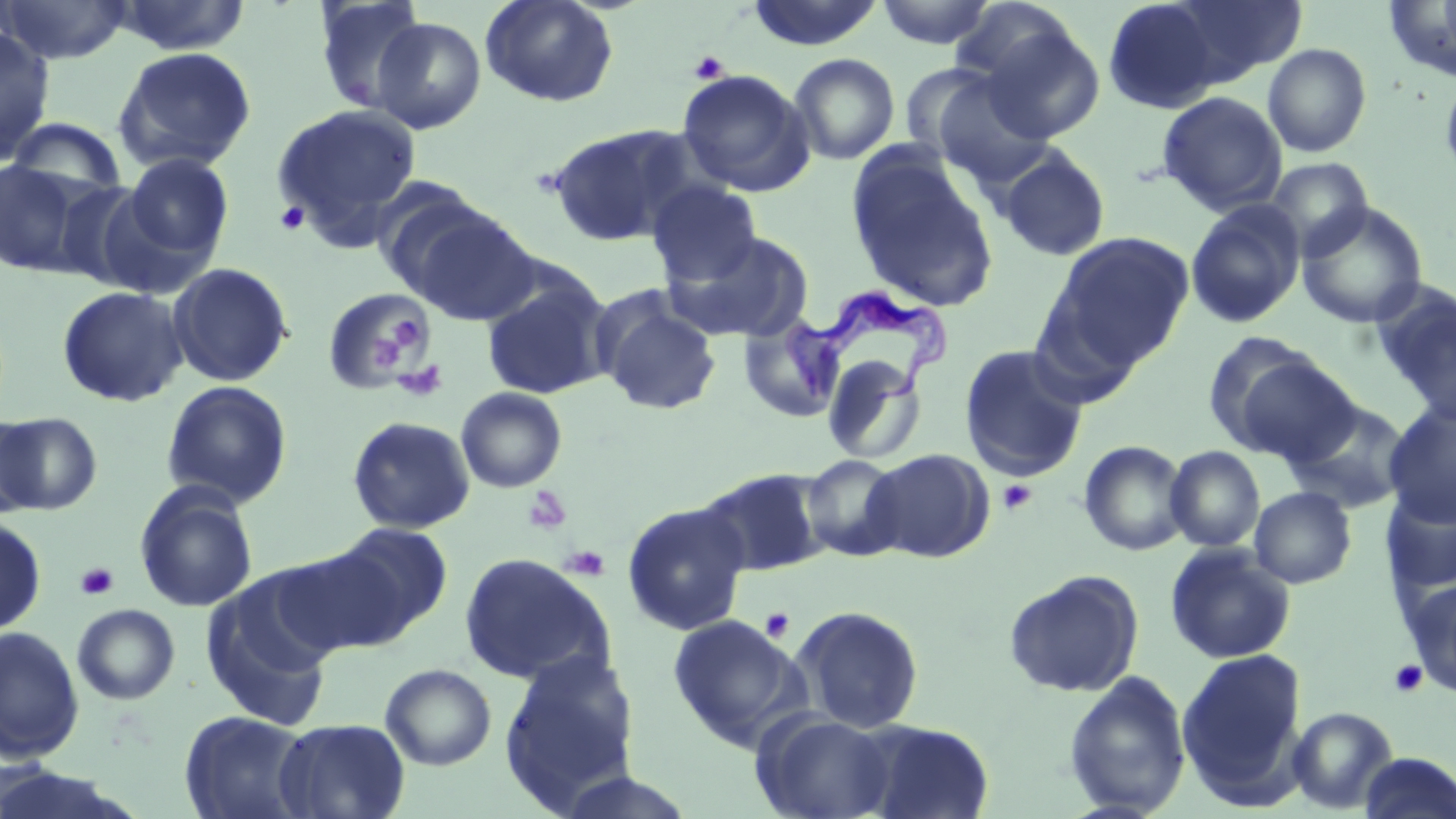
slide-level diagnosis = Trypanosoma brucei
uninfected red blood cell locations = approximate bounding boxes as named x1/y1/x2/y2 corners in pixels: (x1=109, y1=0, x2=252, y2=56), (x1=312, y1=0, x2=431, y2=115), (x1=480, y1=0, x2=619, y2=108), (x1=746, y1=0, x2=883, y2=51), (x1=875, y1=0, x2=996, y2=49), (x1=1102, y1=0, x2=1224, y2=113), (x1=1166, y1=0, x2=1307, y2=84), (x1=0, y1=1, x2=132, y2=64), (x1=950, y1=1, x2=1081, y2=90), (x1=1383, y1=3, x2=1456, y2=82), (x1=370, y1=17, x2=486, y2=134), (x1=0, y1=25, x2=55, y2=165), (x1=980, y1=25, x2=1106, y2=143), (x1=1262, y1=43, x2=1372, y2=158), (x1=113, y1=46, x2=257, y2=174), (x1=788, y1=53, x2=900, y2=165), (x1=1440, y1=66, x2=1456, y2=190), (x1=913, y1=67, x2=1057, y2=185), (x1=677, y1=69, x2=814, y2=196), (x1=1157, y1=91, x2=1287, y2=215), (x1=271, y1=102, x2=422, y2=244), (x1=5, y1=116, x2=129, y2=201), (x1=545, y1=123, x2=701, y2=246), (x1=997, y1=146, x2=1112, y2=260), (x1=846, y1=151, x2=999, y2=313), (x1=121, y1=153, x2=233, y2=265), (x1=1263, y1=156, x2=1374, y2=260), (x1=0, y1=159, x2=88, y2=278), (x1=647, y1=181, x2=762, y2=286), (x1=1185, y1=200, x2=1306, y2=329), (x1=1296, y1=202, x2=1429, y2=328), (x1=402, y1=204, x2=541, y2=325), (x1=667, y1=230, x2=814, y2=343), (x1=1047, y1=230, x2=1195, y2=370), (x1=167, y1=262, x2=294, y2=387), (x1=481, y1=275, x2=614, y2=399), (x1=1372, y1=283, x2=1456, y2=423), (x1=56, y1=285, x2=189, y2=408), (x1=320, y1=286, x2=432, y2=394), (x1=594, y1=293, x2=722, y2=417), (x1=738, y1=312, x2=848, y2=423), (x1=1205, y1=337, x2=1352, y2=463), (x1=958, y1=343, x2=1090, y2=481), (x1=822, y1=354, x2=927, y2=465), (x1=160, y1=380, x2=293, y2=509), (x1=456, y1=387, x2=567, y2=493), (x1=1284, y1=399, x2=1413, y2=515), (x1=1383, y1=402, x2=1456, y2=526), (x1=0, y1=412, x2=41, y2=519), (x1=1, y1=413, x2=101, y2=516), (x1=347, y1=416, x2=475, y2=534), (x1=1078, y1=439, x2=1191, y2=556), (x1=1165, y1=445, x2=1265, y2=551), (x1=862, y1=448, x2=994, y2=562), (x1=801, y1=455, x2=905, y2=561), (x1=697, y1=467, x2=830, y2=578), (x1=134, y1=483, x2=259, y2=614), (x1=1249, y1=486, x2=1357, y2=588), (x1=1381, y1=487, x2=1456, y2=595), (x1=621, y1=501, x2=751, y2=636), (x1=0, y1=517, x2=47, y2=636), (x1=330, y1=523, x2=454, y2=638), (x1=1164, y1=544, x2=1296, y2=664), (x1=273, y1=545, x2=415, y2=656), (x1=458, y1=552, x2=616, y2=687), (x1=1003, y1=569, x2=1145, y2=698), (x1=200, y1=574, x2=338, y2=733), (x1=1406, y1=578, x2=1456, y2=697), (x1=72, y1=603, x2=180, y2=705), (x1=791, y1=605, x2=925, y2=733), (x1=668, y1=614, x2=807, y2=750), (x1=0, y1=626, x2=84, y2=763), (x1=1177, y1=648, x2=1307, y2=805), (x1=499, y1=651, x2=641, y2=811), (x1=380, y1=663, x2=497, y2=770), (x1=1062, y1=670, x2=1192, y2=817), (x1=1287, y1=706, x2=1399, y2=814), (x1=180, y1=710, x2=314, y2=819), (x1=753, y1=712, x2=898, y2=819), (x1=274, y1=719, x2=410, y2=819), (x1=861, y1=719, x2=995, y2=819), (x1=1358, y1=752, x2=1455, y2=819), (x1=0, y1=766, x2=138, y2=817)
image size = 1456×819 pixels
magnification = 1000x
field of view = one of a larger specimen
stain = May-Grünwald-Giemsa
preparation = thin blood smear
modality = light microscopy
platelet locations = approximate bounding boxes as named x1/y1/x2/y2 corners in pixels: (x1=689, y1=50, x2=730, y2=83), (x1=274, y1=201, x2=310, y2=235), (x1=388, y1=316, x2=429, y2=352), (x1=372, y1=330, x2=405, y2=374), (x1=392, y1=360, x2=448, y2=402), (x1=997, y1=480, x2=1038, y2=514), (x1=522, y1=486, x2=572, y2=535), (x1=560, y1=545, x2=610, y2=581), (x1=75, y1=561, x2=119, y2=601), (x1=759, y1=608, x2=795, y2=642), (x1=1388, y1=659, x2=1428, y2=697)
Trypanosoma brucei locations = approximate bounding boxes as named x1/y1/x2/y2 corners in pixels: (x1=776, y1=286, x2=944, y2=409)